Point out each malaria parasite.
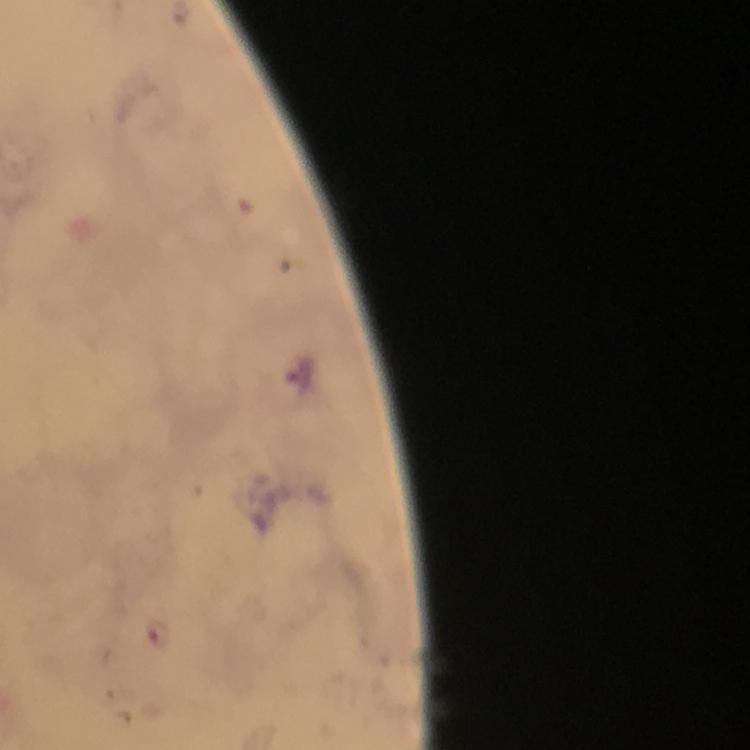

Approximate centers as {x, y} in pixels.
Malaria parasites: {301, 375}, {158, 637}.

100x magnification. Image is 750×750 pixels. Giemsa-stained preparation. Thick blood film. Immersion oil was used. Photographed through the microscope with a smartphone camera. A crop from one field of view. From a malaria diagnostic workup.